Report the malaria status of this cell.
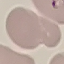
Uninfected.

Summary:
  - Image type: automatically extracted cell patch, resized to 64 × 64 pixels
  - Capture: smartphone through the microscope eyepiece
  - Preparation: thin blood film
  - Stain: Giemsa